Locate every Plasmodium parasite.
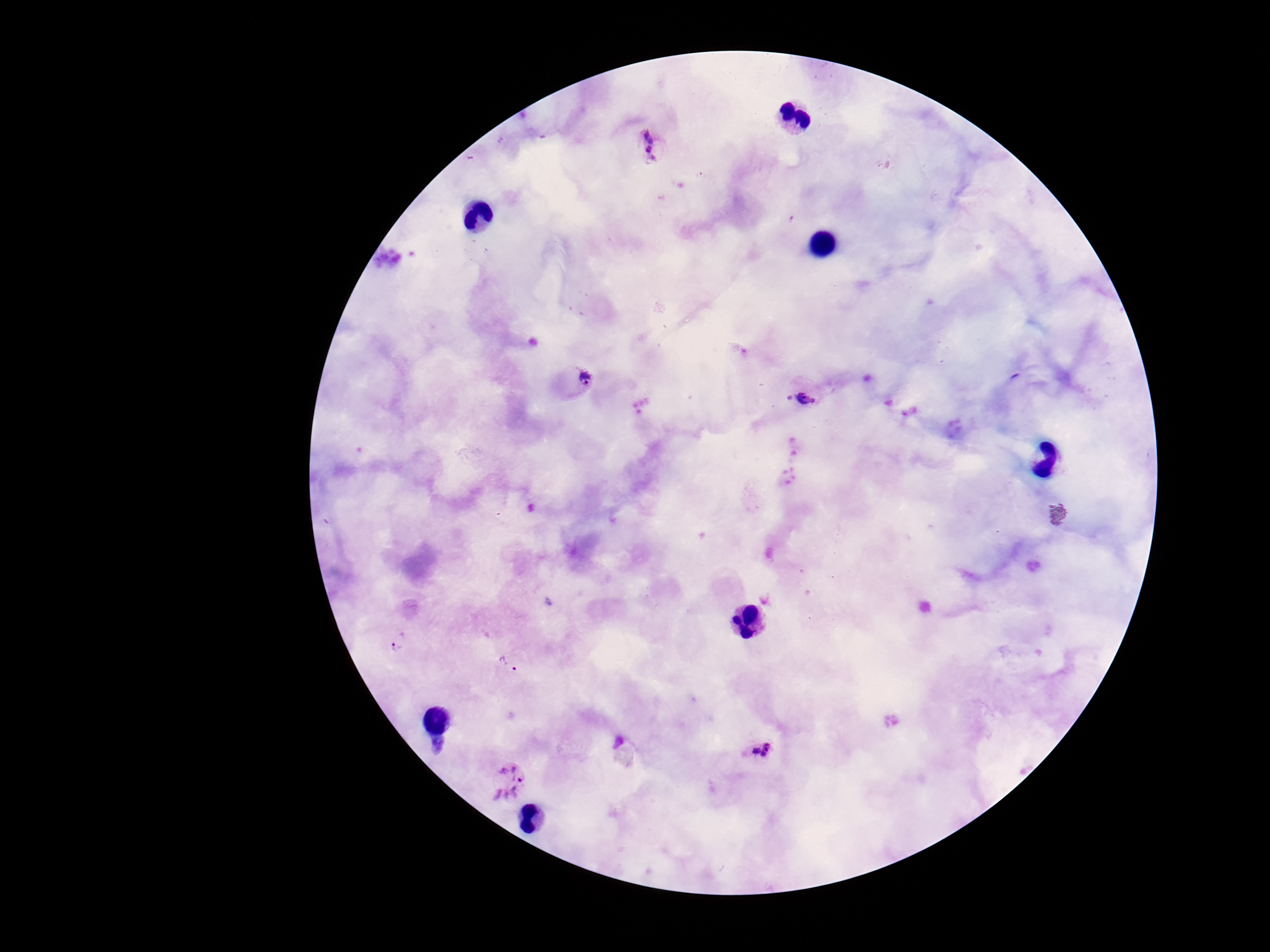
Approximate centers as (x, y) in pixels.
Plasmodium parasites: (654, 145), (574, 381), (806, 398), (397, 640), (509, 663), (760, 754), (507, 785).

Patient malaria status: positive. Smartphone photograph taken through the microscope eyepiece. Single field of view. Giemsa stain. Thick blood film. Image is 1270×952 pixels. 100x magnification.